Name the cell type shown.
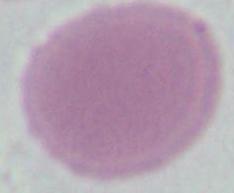

An erythrocyte.

Summary:
  - Magnification: 1000x
  - Modality: micrograph